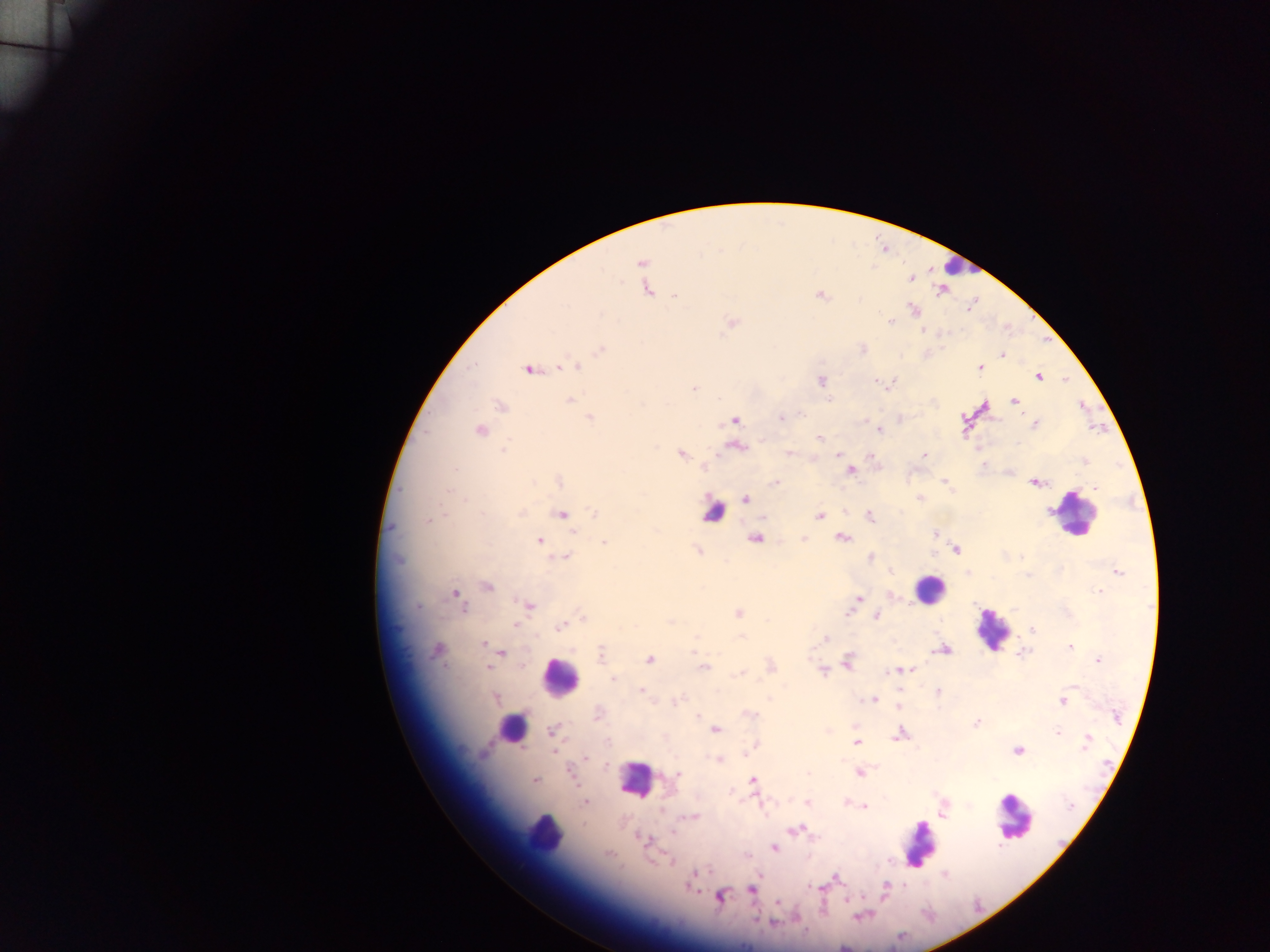
Approximate centers as x y in pixels.
Summary:
  - Plasmodium parasite locations: 642 263; 910 278; 644 279; 647 289; 941 289; 820 295; 674 296; 913 310; 891 322; 731 323; 923 330; 600 349; 1001 355; 562 367; 575 367; 528 368; 980 368; 1037 375; 820 381; 889 384; 694 389; 569 400; 1014 401; 500 406; 589 417; 781 417; 900 418; 734 421; 1034 424; 879 430; 480 431; 819 439; 736 445; 979 448; 680 454; 789 454; 837 454; 923 455; 871 458; 1085 461; 850 471; 1008 471; 559 481; 944 481; 1035 482; 775 483; 919 498; 745 500; 844 512; 561 513; 594 513; 870 515; 819 516; 429 519; 935 534; 755 537; 842 537; 803 538; 540 541; 604 542; 699 550; 955 550; 871 557; 566 558; 891 571; 1117 572; 487 586; 1098 591; 455 593; 892 596; 858 599; 527 604; 851 609; 737 613; 848 613; 875 615; 583 617; 514 624; 561 626; 1031 630; 825 638; 482 643; 1068 646; 436 649; 943 649; 501 652; 695 652; 1022 652; 601 654; 649 660; 1098 660; 846 662; 771 666; 487 667; 703 667; 900 670; 822 671; 739 673; 615 679; 1074 685; 641 690; 938 693; 495 698; 677 700; 873 700; 1062 700; 899 707; 748 714; 597 715; 976 722; 855 725; 715 728; 552 730; 828 730; 898 733; 1058 733; 856 742; 1087 742; 754 744; 553 750; 1017 750; 585 757; 718 759; 859 772; 676 775; 752 779; 534 780; 585 802; 807 802; 757 803; 845 803; 863 806; 942 809; 693 816; 795 830; 640 837; 773 847; 747 854; 669 860; 695 874; 944 874; 838 878; 690 886; 751 889; 884 890; 719 896; 845 899; 777 902; 859 915; 796 917; 773 923; 844 946
  - Leukocyte locations: 958 266; 713 511; 1075 512; 928 589; 993 628; 560 677; 512 727; 635 779; 1013 816; 544 831; 918 843
  - Image size: 1270×952 pixels
  - Preparation: thick blood film
  - Country: Ghana
  - Capture: mobile-phone photograph through a microscope
  - Field of view: single